Mark where platelets are.
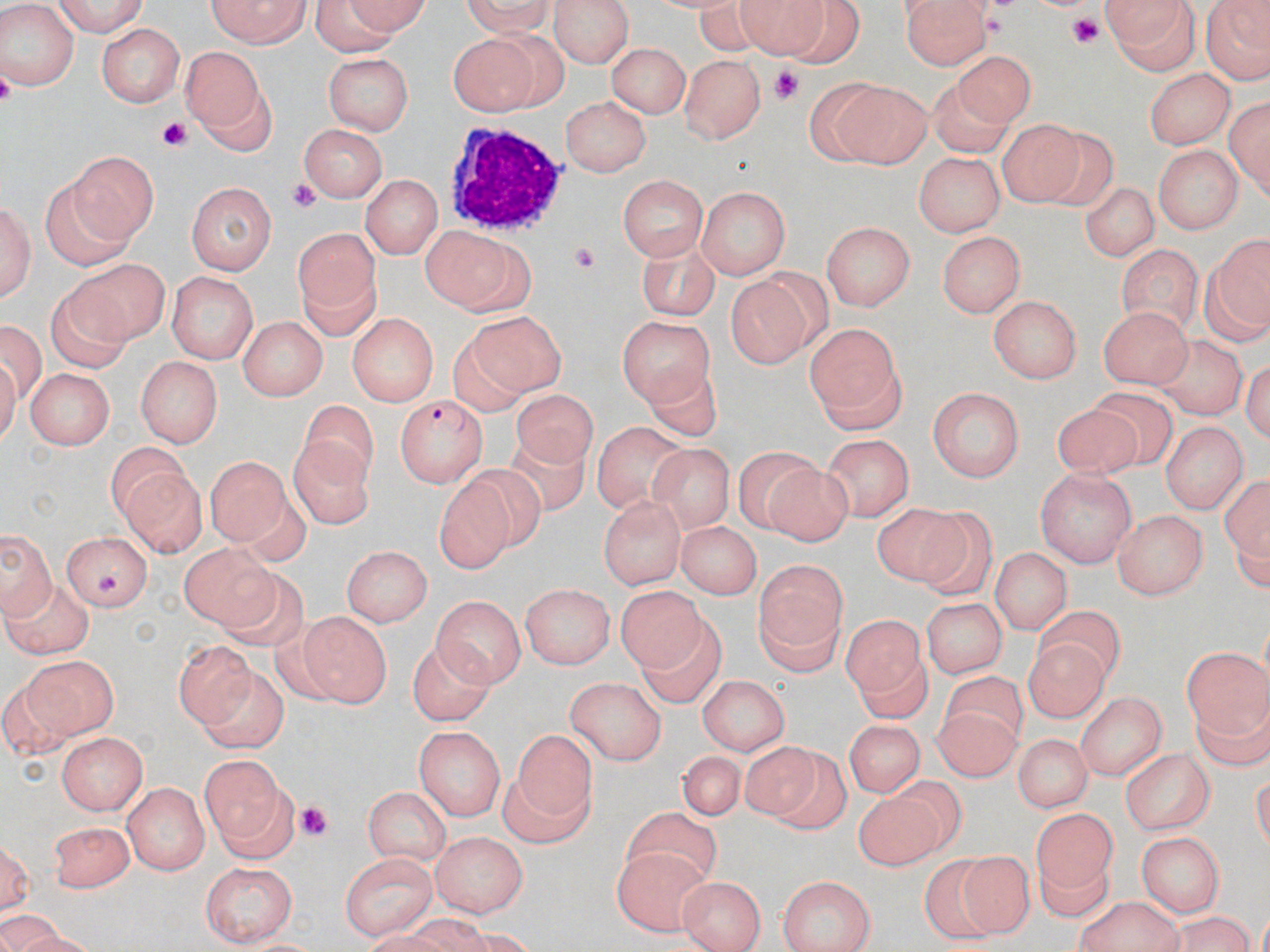

Approximate bounding boxes as [x1, y1, x2, y2] in pixels.
Platelets: [1063, 16, 1107, 48], [767, 65, 801, 103], [158, 119, 193, 149], [285, 181, 321, 214], [566, 243, 600, 275], [96, 571, 125, 601], [297, 804, 331, 842].

Uninfected red blood cell locations: [47, 0, 151, 35], [202, 0, 311, 48], [460, 0, 565, 38], [549, 0, 636, 67], [693, 0, 762, 52], [736, 0, 835, 55], [898, 0, 989, 71], [1099, 0, 1202, 73], [1203, 0, 1268, 85], [306, 1, 438, 50], [780, 1, 866, 69], [0, 7, 81, 89], [98, 24, 182, 107], [483, 29, 572, 109], [449, 32, 539, 113], [609, 42, 688, 121], [183, 45, 267, 139], [326, 51, 415, 134], [956, 53, 1037, 127], [679, 55, 763, 143], [1146, 67, 1231, 150], [834, 75, 932, 167], [927, 75, 1006, 155], [807, 82, 895, 167], [1225, 92, 1268, 205], [560, 97, 651, 174], [997, 118, 1082, 208], [296, 122, 390, 200], [1037, 130, 1122, 210], [1152, 143, 1244, 232], [72, 150, 154, 243], [912, 151, 1003, 237], [360, 173, 441, 262], [617, 173, 706, 265], [47, 178, 135, 272], [186, 180, 275, 273], [1079, 180, 1158, 265], [698, 187, 786, 280], [1, 195, 37, 309], [823, 220, 912, 311], [291, 225, 379, 338], [935, 229, 1027, 318], [423, 233, 512, 309], [1213, 235, 1270, 332], [631, 237, 721, 318], [1115, 247, 1202, 338], [66, 257, 170, 348], [756, 269, 832, 346], [166, 271, 261, 359], [728, 278, 804, 368], [48, 289, 134, 370], [989, 295, 1084, 384], [1095, 306, 1193, 385], [348, 312, 435, 408], [469, 312, 568, 395], [238, 316, 325, 400], [0, 318, 46, 406], [622, 318, 716, 412], [804, 319, 908, 430], [442, 334, 531, 418], [1153, 336, 1244, 417], [133, 358, 223, 448], [645, 361, 722, 439], [27, 367, 114, 448], [927, 385, 1023, 481], [518, 391, 593, 470], [1088, 392, 1178, 468], [301, 400, 379, 490], [1055, 407, 1143, 478], [593, 419, 682, 504], [1161, 420, 1247, 516], [819, 433, 913, 523], [501, 434, 588, 511], [288, 435, 377, 527], [105, 442, 189, 527], [647, 444, 732, 531], [734, 446, 821, 535], [204, 452, 289, 549], [759, 464, 850, 547], [463, 465, 545, 547], [114, 467, 204, 556], [1035, 468, 1135, 567], [437, 478, 513, 571], [1219, 479, 1270, 564], [599, 495, 687, 588], [872, 505, 973, 590], [1112, 508, 1210, 602], [915, 513, 995, 596], [677, 522, 762, 595], [0, 523, 57, 621], [59, 529, 151, 612], [175, 541, 282, 636], [339, 545, 435, 625], [991, 549, 1070, 633], [753, 559, 848, 673], [218, 569, 308, 651], [3, 578, 96, 655], [522, 581, 616, 668], [618, 590, 706, 676], [432, 594, 526, 683], [923, 596, 1006, 680], [1035, 606, 1126, 679], [296, 609, 392, 706], [642, 615, 728, 713], [842, 619, 926, 693], [405, 638, 498, 725], [1027, 639, 1105, 724], [177, 640, 260, 728], [1182, 643, 1269, 724], [854, 651, 938, 717], [5, 654, 116, 756], [199, 667, 290, 750], [944, 670, 1030, 741], [565, 675, 665, 766], [696, 675, 794, 754], [1075, 690, 1165, 783], [1191, 690, 1270, 777], [929, 706, 1019, 781], [844, 717, 925, 795], [415, 728, 503, 821], [59, 729, 145, 811], [514, 729, 605, 819], [1018, 737, 1091, 810], [735, 740, 824, 821], [775, 748, 851, 838], [1119, 750, 1216, 831], [674, 751, 745, 821], [198, 755, 296, 861], [896, 772, 968, 852], [499, 773, 591, 848], [122, 781, 209, 876], [362, 784, 452, 864], [847, 791, 943, 870], [622, 808, 726, 892], [1034, 809, 1113, 889], [49, 815, 137, 890], [2, 829, 38, 923], [1134, 831, 1224, 917], [427, 832, 530, 917], [611, 845, 720, 935], [961, 850, 1029, 935], [1036, 850, 1112, 919], [340, 851, 435, 939], [922, 856, 996, 948], [197, 859, 298, 945], [678, 872, 766, 951], [777, 874, 877, 952], [1073, 897, 1183, 951]. White blood cell locations: [444, 118, 565, 234]. Plasmodium falciparum-infected red blood cell locations: [394, 394, 490, 486]. Slide-level diagnosis: Plasmodium falciparum. Light microscopy. Image is 1270×952 pixels. Thin blood film. One field of a larger specimen. Captured at 1000x magnification. May-Grünwald-Giemsa stain.